Give the extent of all white blood cells.
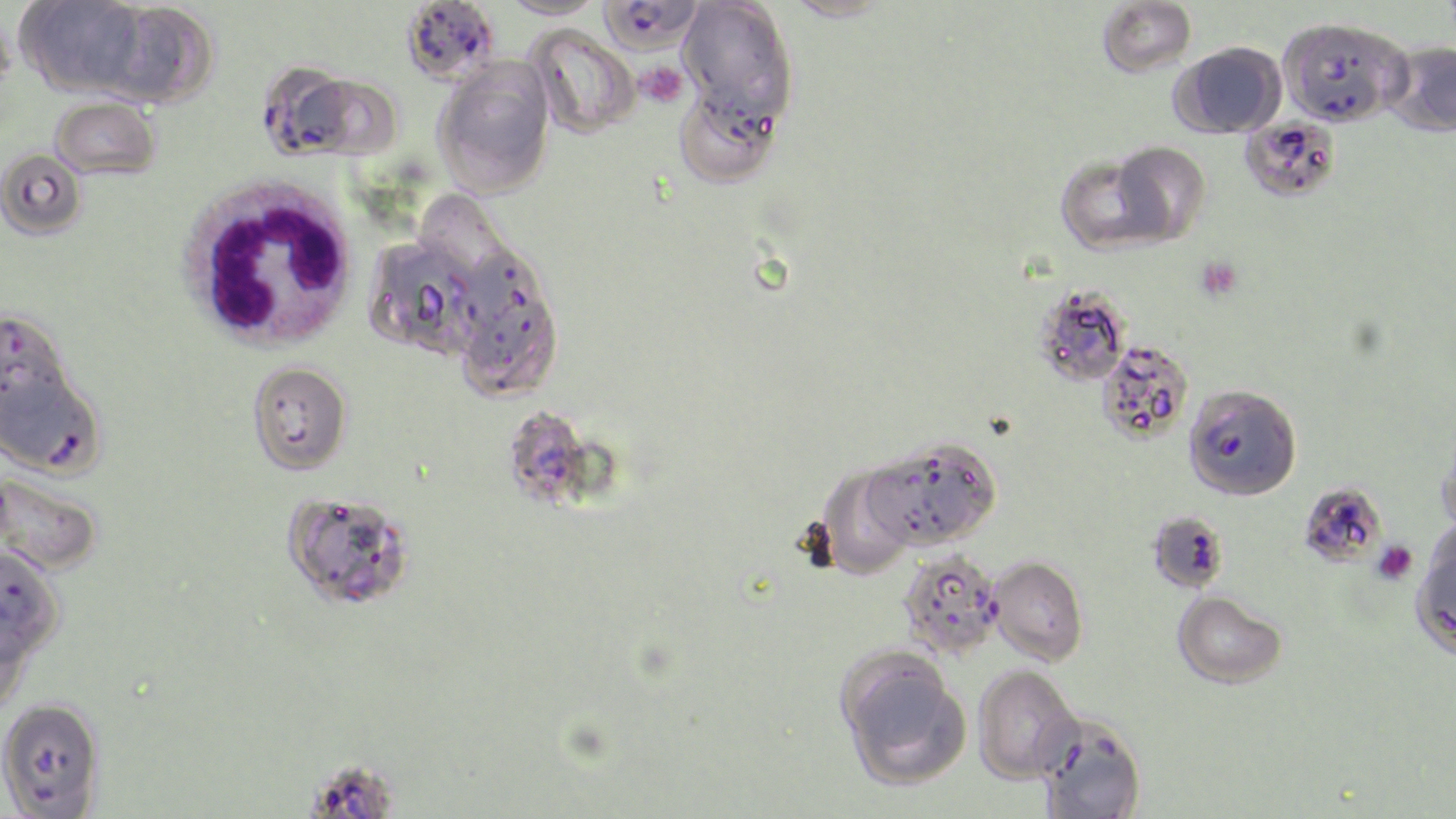

Approximate bounding boxes as (x1, y1, x2, y2) in pixels.
White blood cells: (176, 174, 364, 354).

slide-level diagnosis = Plasmodium falciparum
uninfected red blood cell locations = approximate bounding boxes as (x1, y1, x2, y2) in pixels: (783, 0, 897, 23), (1097, 0, 1197, 78), (16, 1, 150, 99), (500, 1, 607, 20), (678, 1, 798, 124), (101, 2, 218, 108), (525, 25, 640, 139), (1383, 41, 1456, 138), (1171, 42, 1286, 139), (433, 57, 555, 197), (673, 84, 783, 189), (51, 96, 161, 179), (1239, 117, 1341, 203), (1110, 141, 1211, 246), (0, 149, 86, 241), (1054, 151, 1171, 255), (369, 237, 483, 360), (456, 251, 563, 399), (1033, 285, 1132, 387), (1097, 340, 1194, 444), (246, 361, 352, 475), (1438, 421, 1456, 539), (866, 437, 1002, 550), (814, 464, 918, 580), (0, 471, 104, 576), (282, 490, 416, 612), (988, 555, 1088, 666), (1172, 590, 1287, 689), (0, 612, 33, 720), (835, 647, 970, 790), (973, 664, 1081, 783), (0, 697, 105, 817), (1035, 713, 1147, 819)
field of view = single
Plasmodium falciparum-infected red blood cell locations = approximate bounding boxes as (x1, y1, x2, y2) in pixels: (401, 0, 501, 85), (598, 0, 704, 54), (1278, 17, 1409, 127), (257, 64, 384, 161), (0, 310, 72, 410), (1, 369, 107, 479), (1183, 384, 1302, 501), (501, 405, 609, 512), (1298, 481, 1387, 568), (1146, 509, 1230, 593), (1409, 531, 1456, 662), (0, 545, 65, 664), (898, 551, 1004, 658), (307, 767, 392, 819)
magnification = 1000x
platelet locations = approximate bounding boxes as (x1, y1, x2, y2) in pixels: (637, 62, 688, 108), (1195, 257, 1242, 301), (1372, 539, 1417, 585)
image size = 1456×819 pixels
stain = May-Grünwald-Giemsa
modality = optical microscopy
preparation = thin blood smear